Comment on the morphology of the erythrocytes.
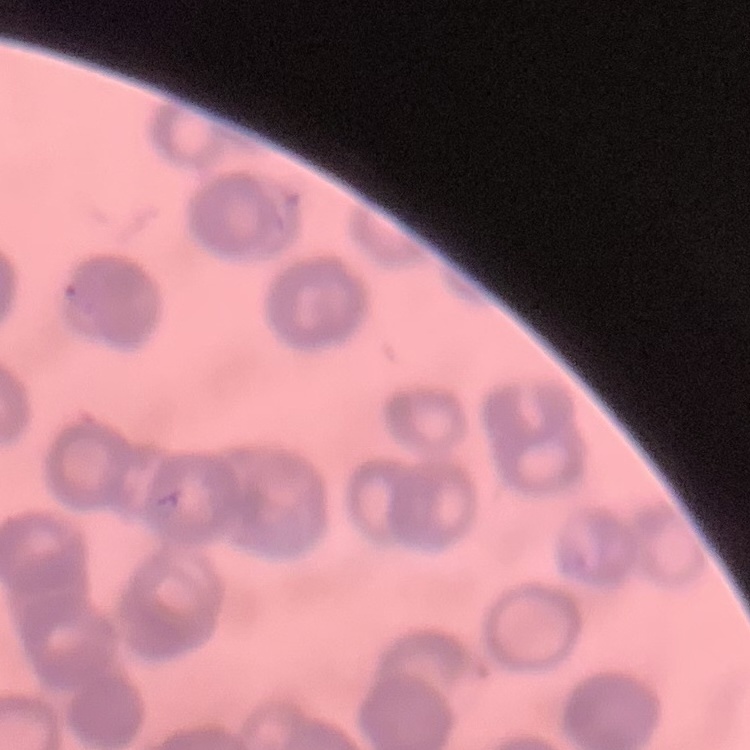

Rouleaux formation.

Thin blood smear. Field's or Giemsa stain. One tile cut from a larger photomicrograph.